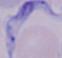
Summary:
  - Magnification: 1000x
  - Modality: photomicrograph
  - Identification: trypanosome